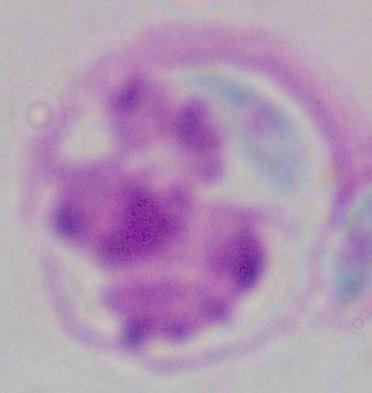
Summary:
  - Magnification: 1000x
  - Modality: micrograph
  - Identification: white blood cell